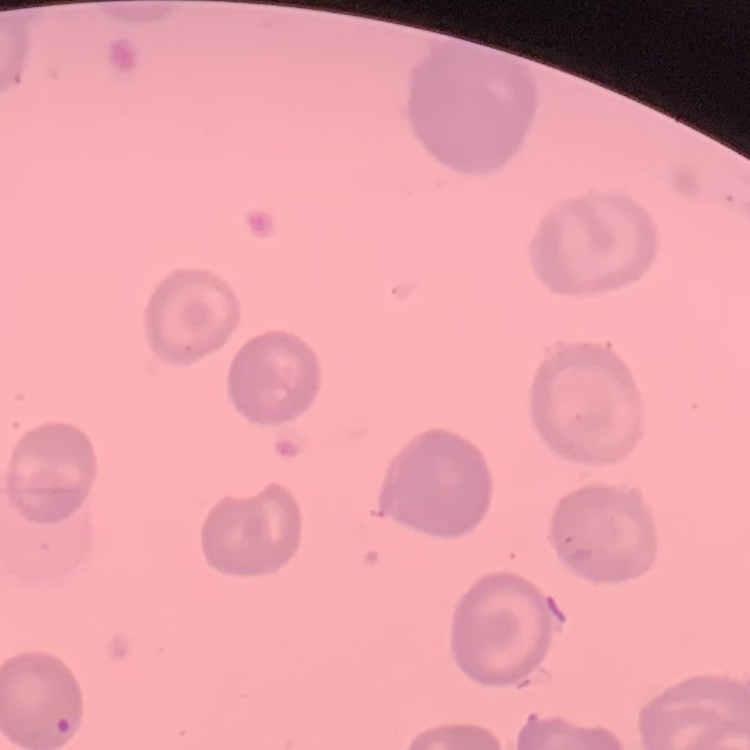

The red blood cells exhibit no rouleaux formation. Thin blood film. Square crop of a larger photomicrograph. Stained with either Field's or Giemsa.